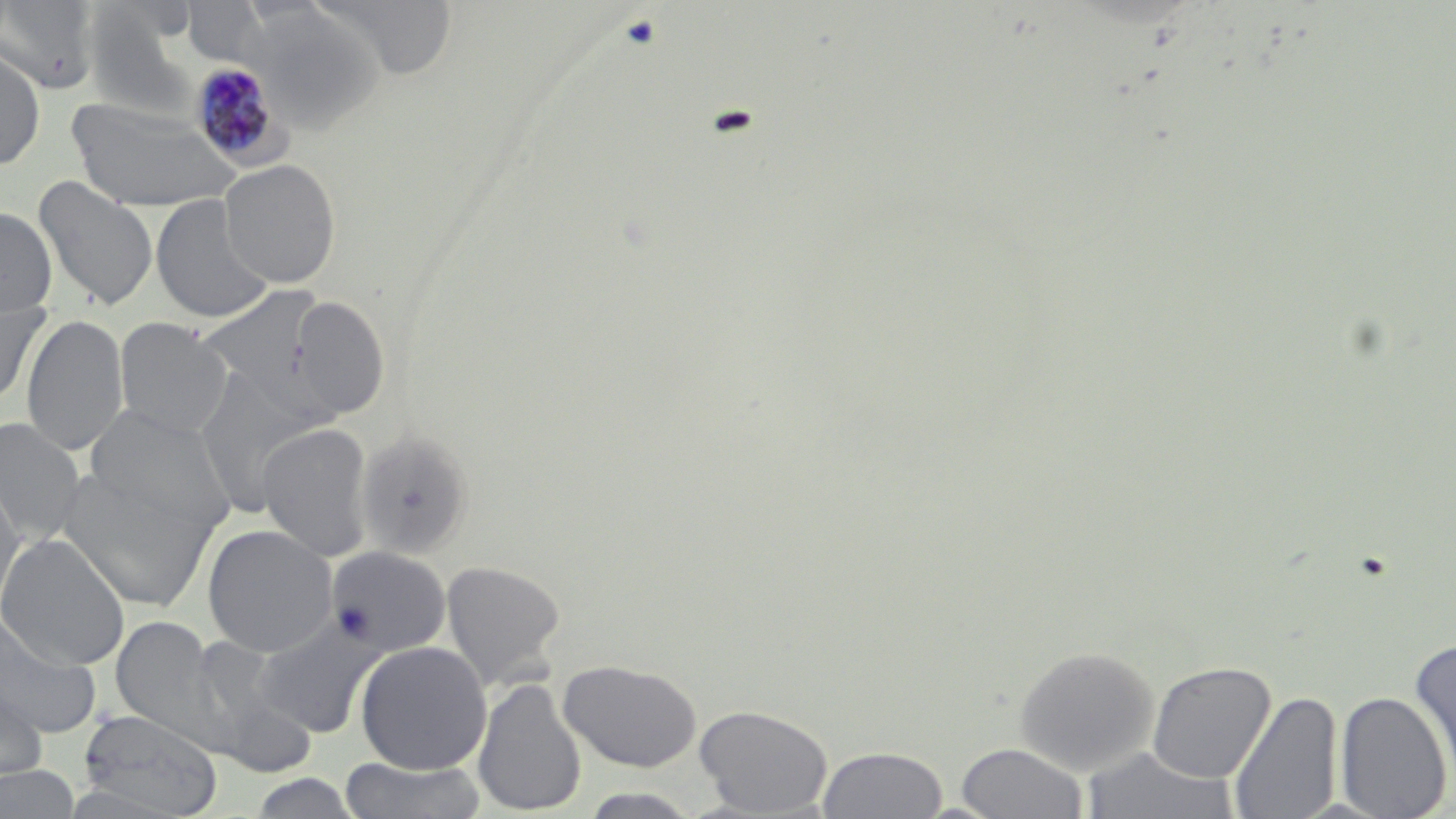 Approximate bounding boxes as [x1, y1, x2, y2] in pixels. Uninfected red blood cell locations: [311, 0, 461, 81], [0, 1, 100, 95], [180, 2, 271, 70], [245, 6, 381, 133], [87, 11, 202, 120], [0, 48, 46, 170], [66, 97, 241, 212], [219, 159, 341, 288], [33, 175, 158, 312], [150, 195, 275, 324], [0, 207, 57, 320], [198, 285, 330, 409], [288, 295, 390, 420], [0, 297, 49, 411], [22, 314, 129, 457], [113, 318, 232, 438], [193, 376, 314, 519], [84, 404, 235, 537], [0, 417, 87, 546], [257, 422, 374, 561], [356, 430, 474, 559], [56, 466, 217, 611], [0, 477, 26, 617], [203, 525, 338, 657], [0, 533, 130, 671], [326, 546, 452, 656], [441, 560, 566, 690], [0, 614, 102, 738], [110, 616, 224, 747], [252, 618, 380, 737], [183, 633, 307, 762], [1408, 638, 1456, 793], [355, 641, 492, 775], [1014, 644, 1159, 776], [558, 659, 703, 772], [1147, 661, 1276, 784], [0, 676, 49, 785], [472, 677, 588, 817], [1228, 689, 1343, 819], [1335, 690, 1452, 819], [695, 704, 834, 817], [77, 711, 224, 817], [956, 742, 1087, 818], [817, 746, 948, 818], [1080, 746, 1239, 819], [338, 756, 488, 818], [0, 765, 81, 818], [245, 772, 363, 817], [577, 788, 704, 818]. Plasmodium malariae-infected red blood cell locations: [189, 61, 287, 167]. Slide-level diagnosis: Plasmodium malariae. Thin blood film. One field of a larger specimen. May-Grünwald-Giemsa-stained preparation. 1000x magnification. Image is 1456×819 pixels. Optical microscopy.